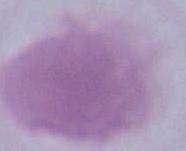
Summary:
  - Modality: micrograph
  - Magnification: 1000x
  - Identification: erythrocyte